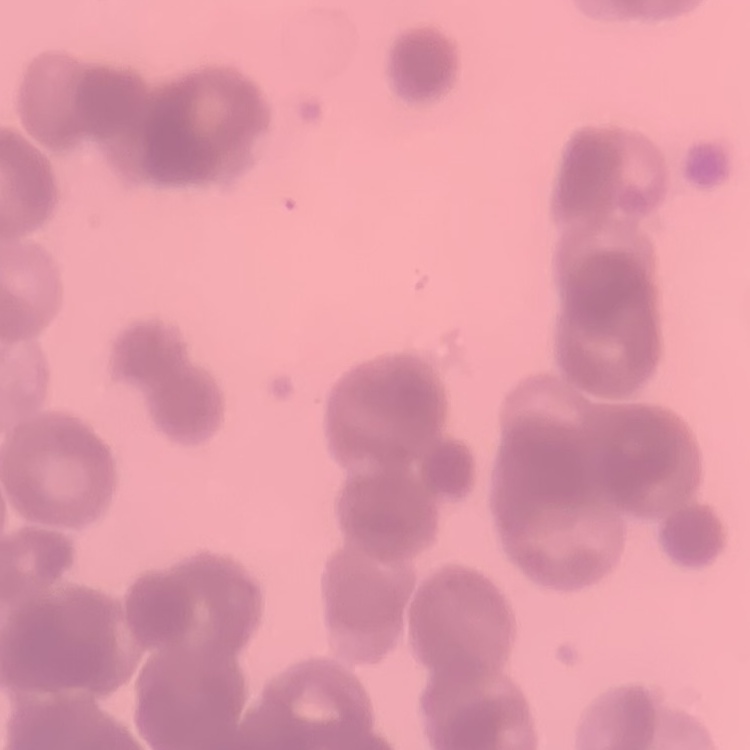

erythrocyte_morphology: rouleaux formation
preparation: thin blood smear
image_type: one tile cut from a larger photomicrograph
stain: Field's or Giemsa